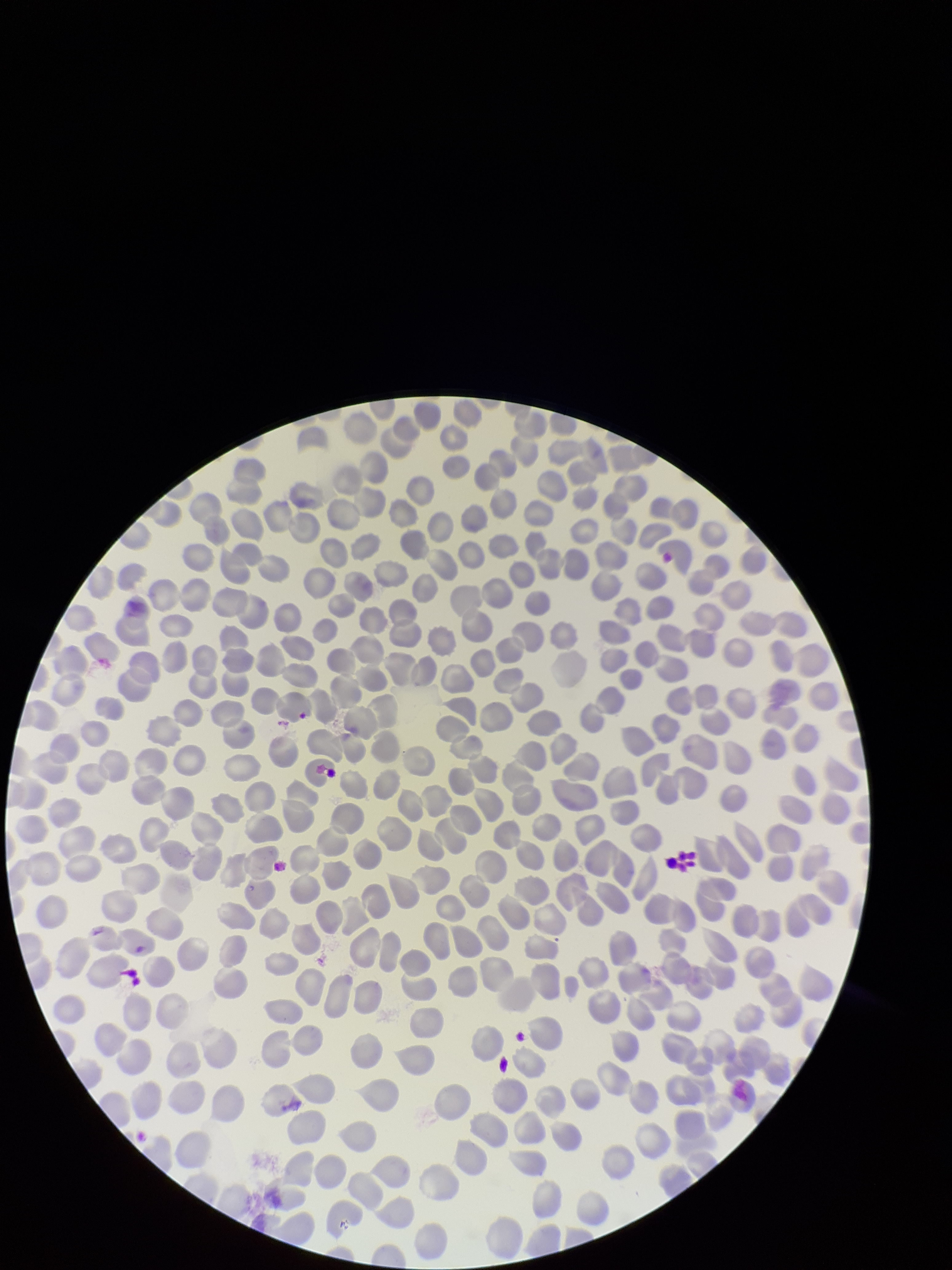

Summary:
  - Parasitized red blood cell count: 0
  - Capture: smartphone photograph through the microscope eyepiece
  - Parasitized red blood cells: none identified
  - Red blood cell count: 355
  - Stain: Giemsa
  - Preparation: thin smear
  - Field of view: single
  - Image size: 952×1270 pixels
  - Patient malaria status: negative